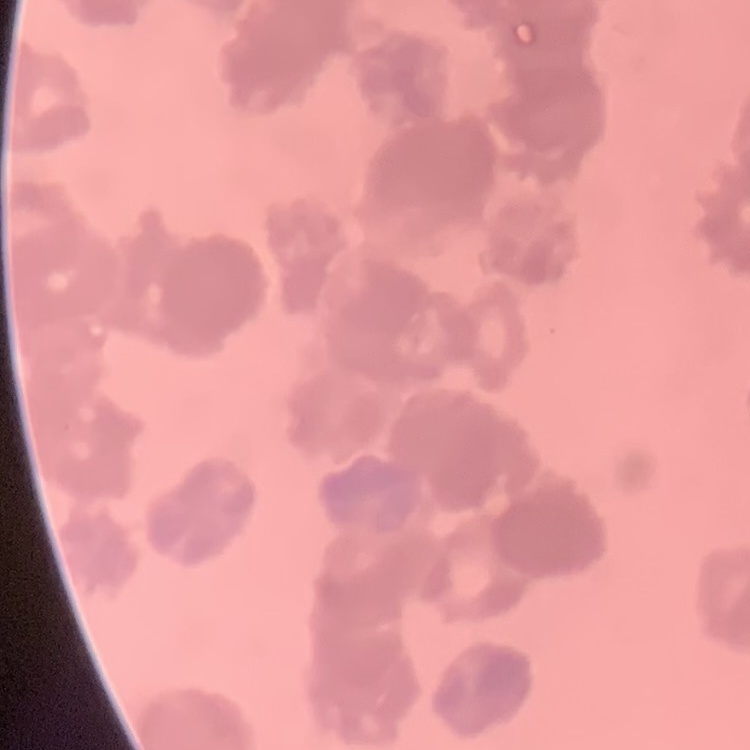 The red blood cells exhibit rouleaux formation. Square crop of a larger photomicrograph. Field's or Giemsa stain. Thin peripheral smear.